Report the malaria status.
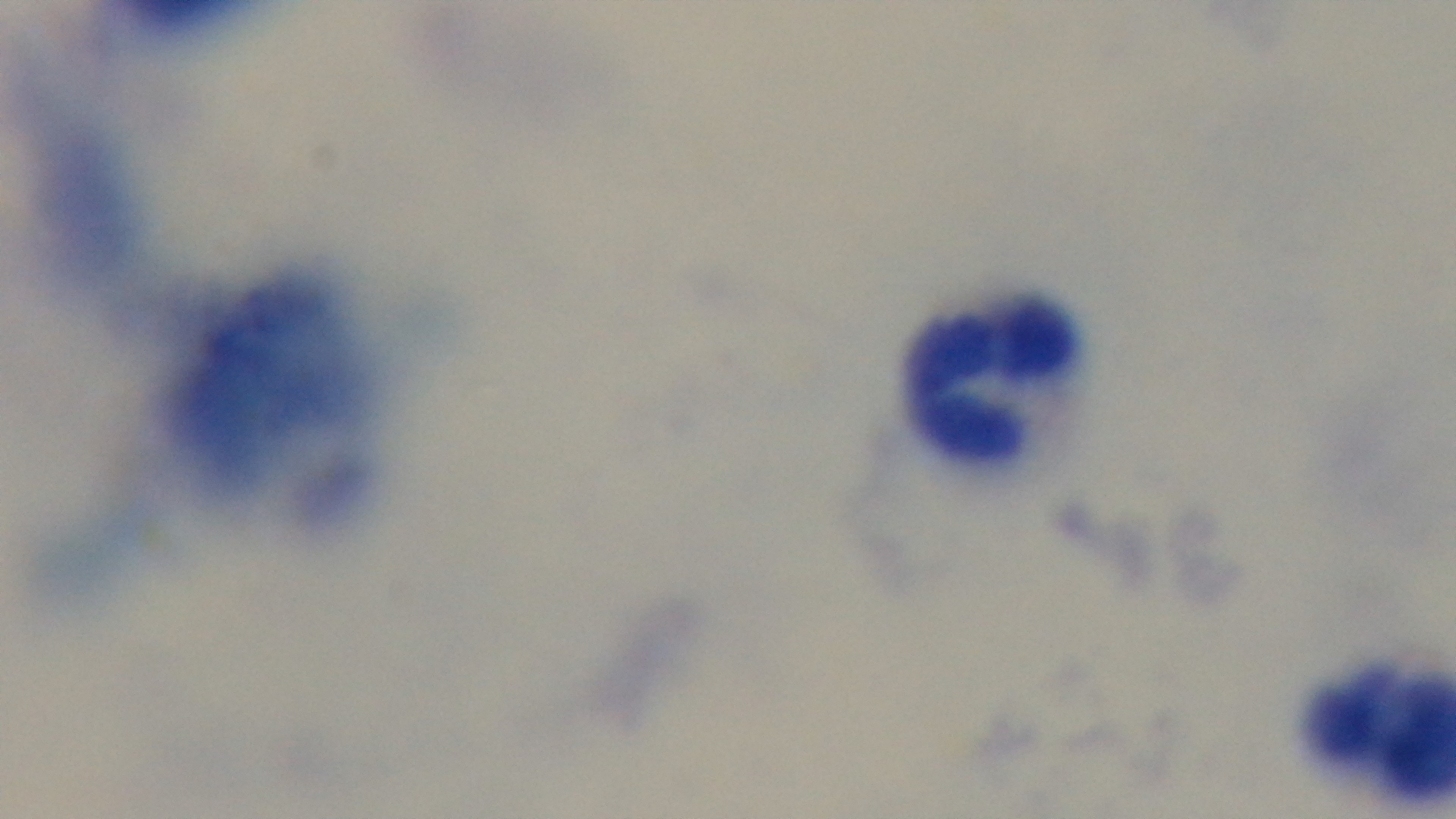
It is uninfected.

modality: light microscopy
capture: mounted 4K digital camera
objective: 100x oil immersion
stain: Giemsa
field_of_view: one from the slide
preparation: thick